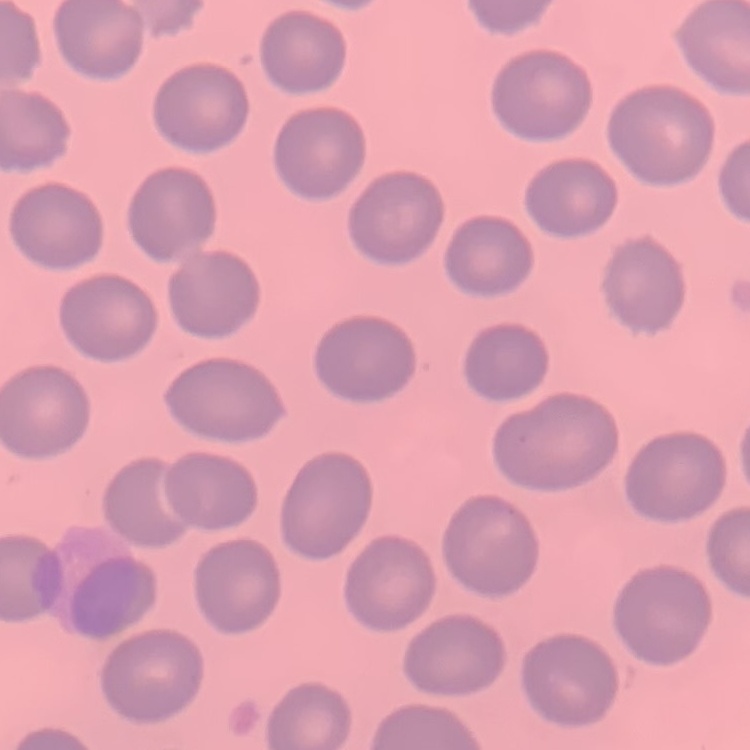

Summary:
  - Erythrocyte morphology: no rouleaux formation
  - Preparation: thin peripheral smear
  - Image type: one tile cut from a larger photomicrograph
  - Stain: Field's or Giemsa